Classify this cell by malaria status.
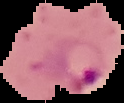

Parasitized.

{
  "image_type": "segmented cell region with the area outside set to black",
  "preparation": "thin blood film",
  "image_size": "124×103 pixels"
}